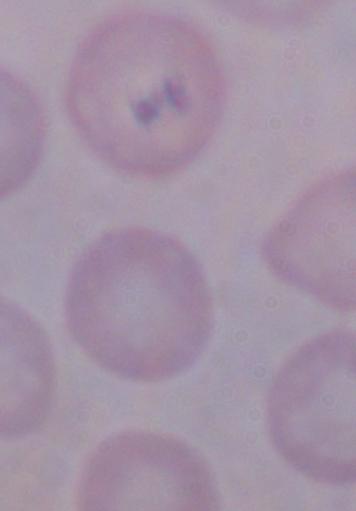

{
  "identification": "trypanosome",
  "magnification": "1000x",
  "modality": "photomicrograph"
}